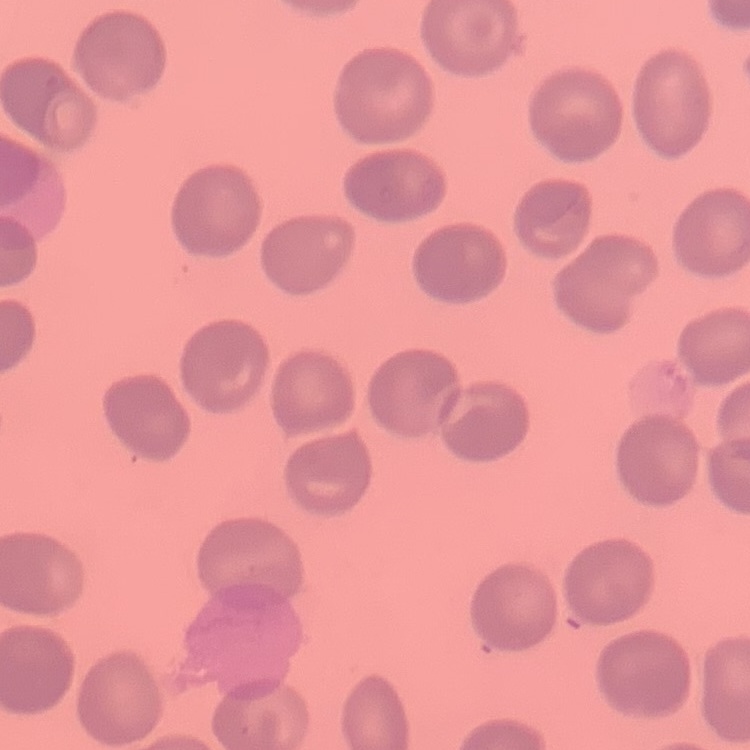
Summary:
  - Red blood cell morphology: no rouleaux formation
  - Stain: Field's or Giemsa
  - Preparation: thin peripheral smear
  - Image type: square crop of a larger photomicrograph